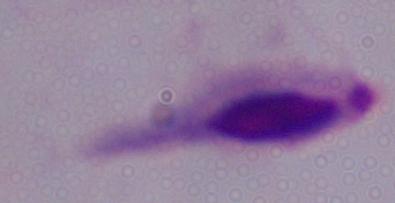
Summary:
  - Magnification: 1000x
  - Modality: photomicrograph
  - Identification: trichomonad